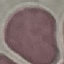 Malaria status: uninfected. Cell patch, automatically extracted from a larger field of view and resized to 64 × 64 pixels. Acquired by smartphone through the microscope eyepiece. Giemsa-stained preparation. Thin blood smear.